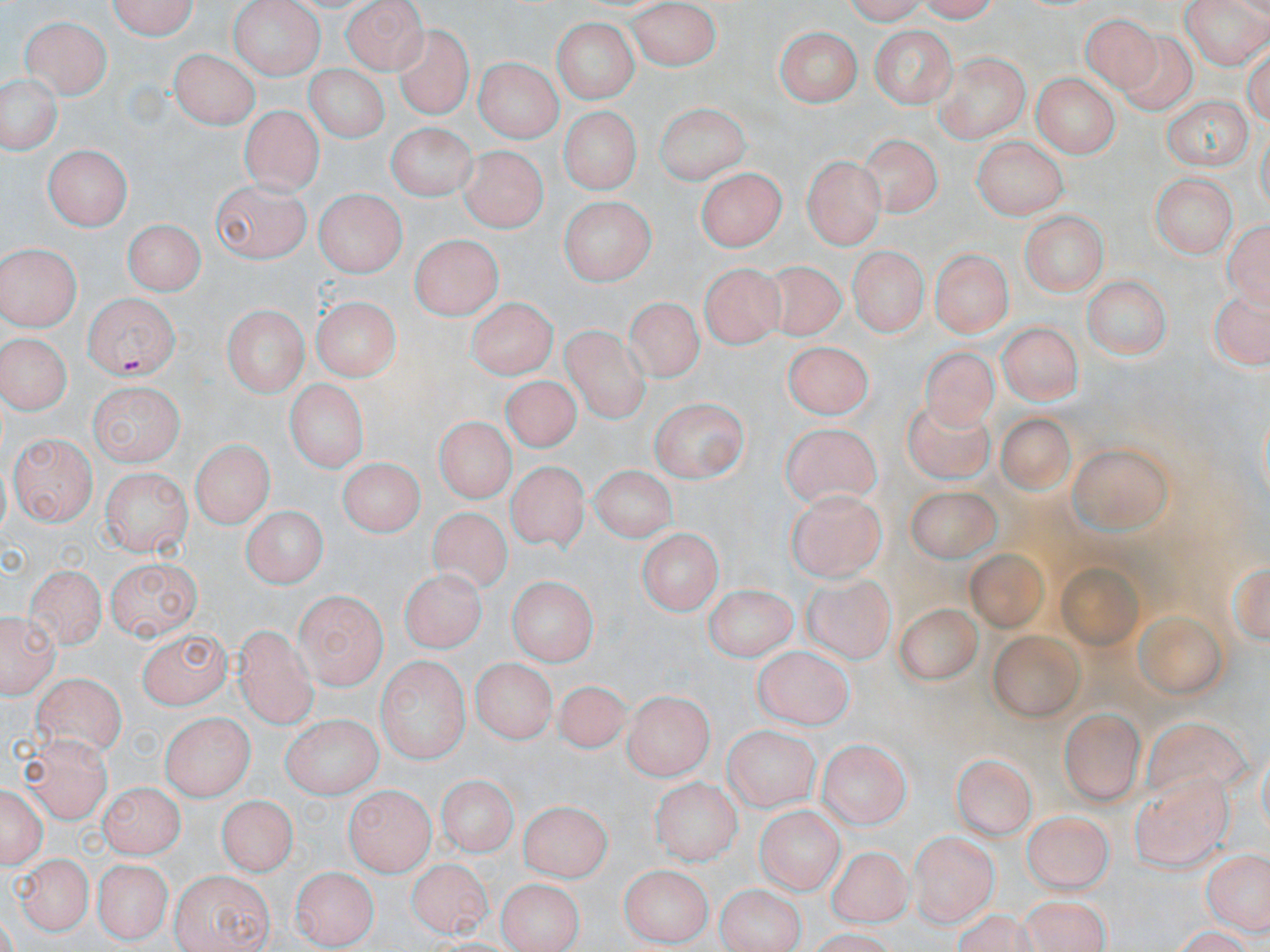
Summary:
  - Coordinate format: approximate bounding boxes as [x1, y1, x2, y2] in pixels
  - Uninfected red blood cell locations: [102, 0, 200, 38], [228, 0, 324, 78], [339, 0, 427, 71], [908, 0, 1009, 24], [1179, 0, 1268, 70], [628, 2, 722, 71], [1080, 8, 1166, 88], [19, 12, 112, 100], [549, 17, 641, 104], [390, 24, 477, 121], [866, 24, 957, 106], [771, 27, 863, 106], [170, 46, 258, 128], [933, 52, 1029, 143], [476, 59, 559, 145], [301, 61, 389, 146], [0, 71, 61, 157], [1030, 74, 1118, 158], [1162, 93, 1252, 168], [653, 103, 750, 180], [241, 105, 322, 194], [559, 108, 640, 194], [386, 125, 472, 201], [860, 130, 943, 210], [970, 139, 1068, 219], [45, 141, 131, 232], [462, 144, 546, 232], [803, 154, 887, 250], [696, 168, 785, 254], [1153, 172, 1235, 255], [209, 178, 306, 260], [316, 189, 403, 279], [556, 197, 657, 284], [1020, 211, 1108, 294], [1226, 215, 1270, 310], [125, 218, 202, 297], [408, 233, 504, 321], [1, 243, 82, 331], [849, 243, 926, 335], [934, 244, 1009, 338], [752, 259, 846, 341], [703, 261, 785, 348], [1081, 277, 1172, 361], [1206, 290, 1270, 371], [308, 296, 400, 382], [625, 296, 702, 381], [466, 298, 557, 380], [222, 306, 307, 399], [996, 321, 1084, 405], [563, 324, 652, 422], [2, 331, 74, 413], [780, 340, 872, 418], [914, 342, 1003, 437], [502, 376, 589, 455], [286, 379, 366, 476], [90, 382, 181, 466], [650, 396, 747, 483], [898, 404, 997, 484], [997, 407, 1079, 502], [428, 414, 522, 506], [777, 422, 881, 503], [9, 434, 95, 525], [191, 438, 272, 531], [1068, 444, 1172, 535], [335, 458, 422, 541], [593, 461, 677, 540], [506, 462, 589, 550], [104, 466, 191, 558], [898, 483, 1004, 566], [785, 490, 885, 585], [239, 506, 328, 588], [427, 508, 514, 596], [639, 527, 719, 614], [965, 546, 1049, 633], [107, 555, 202, 641], [25, 562, 106, 647], [401, 571, 483, 650], [507, 577, 596, 668], [800, 578, 900, 663], [703, 585, 795, 659], [296, 589, 385, 686], [894, 599, 982, 696], [3, 617, 56, 696], [991, 626, 1081, 723], [236, 627, 316, 727], [137, 628, 233, 705], [754, 647, 853, 731], [376, 655, 470, 766], [473, 659, 553, 747], [33, 671, 126, 756], [552, 681, 631, 754], [622, 690, 710, 778], [1057, 703, 1146, 805], [163, 711, 255, 800], [1142, 716, 1250, 800], [283, 718, 380, 800], [722, 724, 817, 810], [816, 735, 910, 830], [25, 737, 110, 822], [951, 756, 1033, 843], [1130, 770, 1229, 870], [435, 774, 517, 859], [652, 774, 743, 864], [2, 781, 45, 870], [102, 783, 181, 857], [343, 786, 430, 873], [217, 795, 292, 876], [517, 800, 614, 878], [756, 804, 841, 897], [1027, 810, 1114, 890], [907, 831, 995, 929], [824, 848, 918, 929], [1204, 852, 1268, 936], [13, 854, 89, 937], [94, 857, 169, 945], [407, 858, 487, 937], [620, 864, 713, 945], [292, 865, 377, 949], [170, 869, 275, 951], [496, 877, 581, 952], [714, 881, 806, 952], [1009, 895, 1110, 952], [951, 909, 1036, 952]
  - Plasmodium falciparum-infected red blood cell locations: [81, 291, 178, 379]
  - Slide-level diagnosis: Plasmodium falciparum
  - Image size: 1270×952 pixels
  - Magnification: 1000x
  - Preparation: thin blood smear
  - Field of view: single
  - Modality: light microscopy
  - Stain: May-Grünwald-Giemsa